Name the blood parasite species.
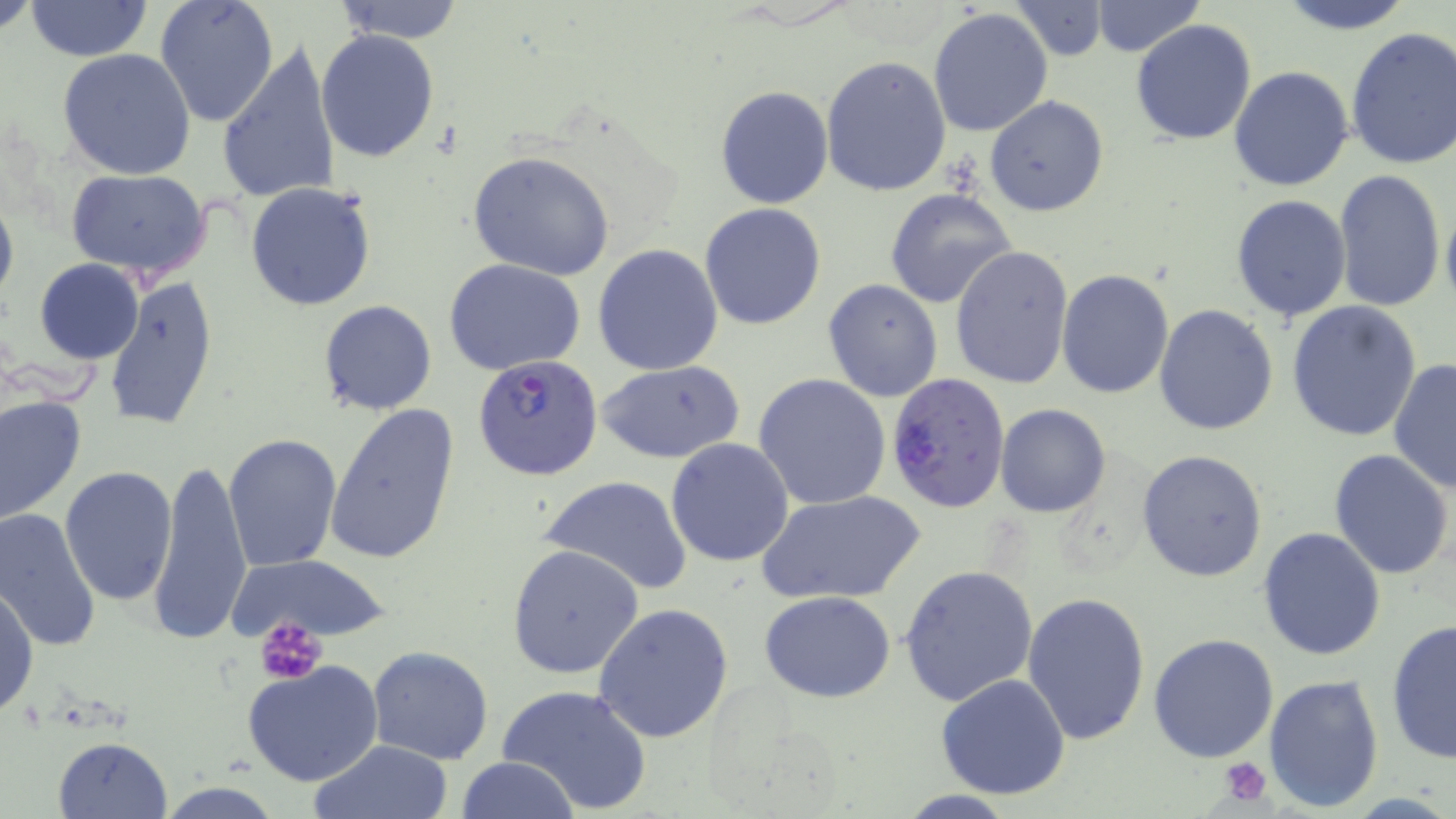
Plasmodium falciparum.

magnification = 1000x
stain = May-Grünwald-Giemsa
uninfected red blood cell locations = approximate bounding boxes as [x1, y1, x2, y2] in pixels: [1, 0, 39, 37], [24, 0, 151, 60], [155, 0, 279, 127], [331, 0, 468, 43], [1274, 0, 1419, 34], [1088, 1, 1207, 57], [1009, 2, 1110, 60], [928, 7, 1053, 137], [1130, 19, 1258, 146], [1345, 26, 1456, 170], [316, 30, 440, 161], [216, 37, 343, 208], [58, 47, 198, 180], [820, 55, 951, 197], [1228, 66, 1355, 192], [716, 87, 833, 209], [985, 96, 1109, 218], [469, 151, 616, 281], [62, 168, 214, 278], [1332, 168, 1447, 313], [245, 182, 377, 312], [0, 186, 18, 311], [884, 188, 1017, 309], [1440, 191, 1456, 316], [1230, 194, 1353, 322], [699, 202, 827, 331], [592, 244, 724, 377], [950, 245, 1074, 388], [442, 257, 586, 377], [34, 259, 144, 365], [1057, 269, 1174, 398], [103, 274, 220, 432], [823, 278, 943, 401], [1286, 299, 1423, 442], [317, 300, 439, 416], [1153, 304, 1279, 434], [1388, 358, 1455, 492], [595, 361, 745, 463], [753, 373, 891, 509], [0, 395, 86, 525], [323, 401, 462, 566], [995, 404, 1110, 517], [223, 434, 344, 573], [665, 438, 795, 567], [1329, 448, 1454, 579], [1136, 449, 1268, 582], [150, 457, 252, 649], [60, 466, 178, 605], [538, 475, 695, 596], [758, 490, 923, 605], [0, 509, 103, 656], [1258, 527, 1387, 662], [507, 545, 645, 680], [223, 554, 392, 644], [899, 564, 1038, 707], [0, 585, 38, 720], [759, 591, 897, 703], [1021, 592, 1150, 746], [593, 603, 735, 744], [1386, 618, 1456, 765], [1148, 632, 1279, 762], [367, 646, 494, 766], [243, 661, 385, 787], [935, 673, 1071, 800], [1262, 673, 1384, 814], [497, 683, 653, 815], [52, 736, 174, 819], [310, 740, 455, 819], [456, 756, 581, 818], [895, 791, 1021, 819]
image size = 1456×819 pixels
field of view = single
Plasmodium falciparum-infected red blood cell locations = approximate bounding boxes as [x1, y1, x2, y2] in pixels: [472, 355, 603, 479], [884, 372, 1011, 513]
platelet locations = approximate bounding boxes as [x1, y1, x2, y2] in pixels: [257, 619, 328, 686], [1216, 755, 1275, 807]
modality = optical microscopy
preparation = thin blood smear